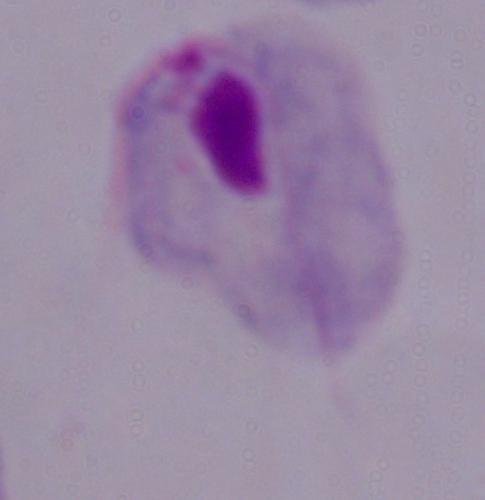
Summary:
  - Modality: photomicrograph
  - Identification: trichomonad
  - Magnification: 1000x